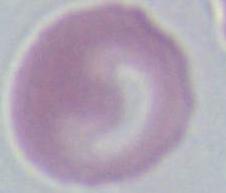

Summary:
  - Identification: erythrocyte
  - Magnification: 1000x
  - Modality: micrograph